Assess this cell for malaria.
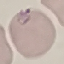

It is parasitized.

capture = smartphone through the microscope eyepiece
image type = automatically extracted cell patch, resized to 64 × 64 pixels
stain = Giemsa
preparation = thin smear